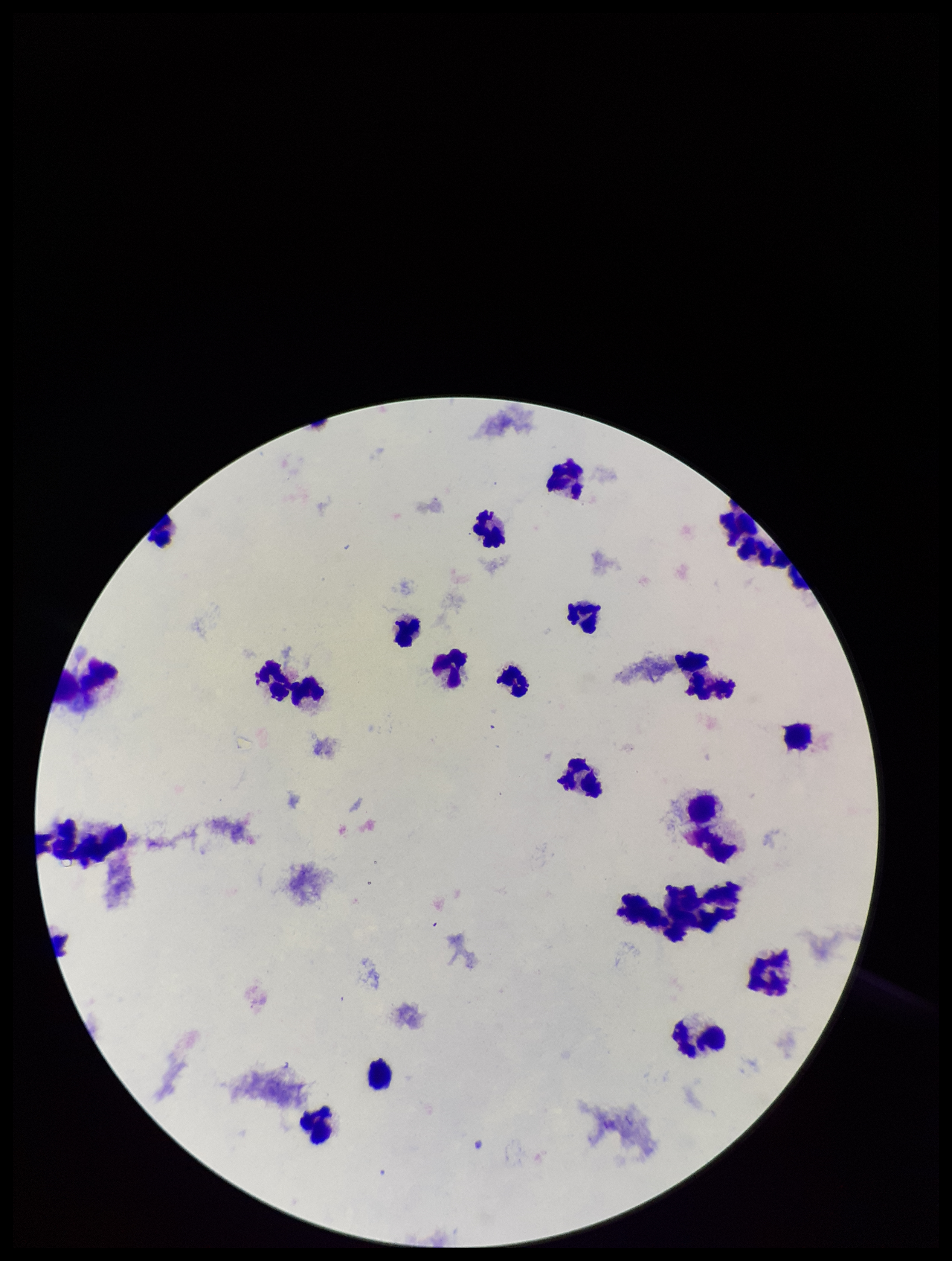
Plasmodium parasites: none seen. Leukocyte count: 22. Parasite count: 0. Image is 952×1261 pixels. Single field of view. Preparation: thick blood smear. Photographed through the microscope eyepiece with a smartphone camera. Stained with Giemsa. Patient malaria status: negative.